Assess this cell for malaria.
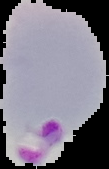
Parasitized.

preparation = thin blood smear
image type = segmented cell region with the area outside set to black
image size = 109×169 pixels